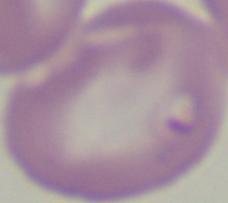

Summary:
  - Modality: micrograph
  - Magnification: 1000x
  - Identification: Babesia